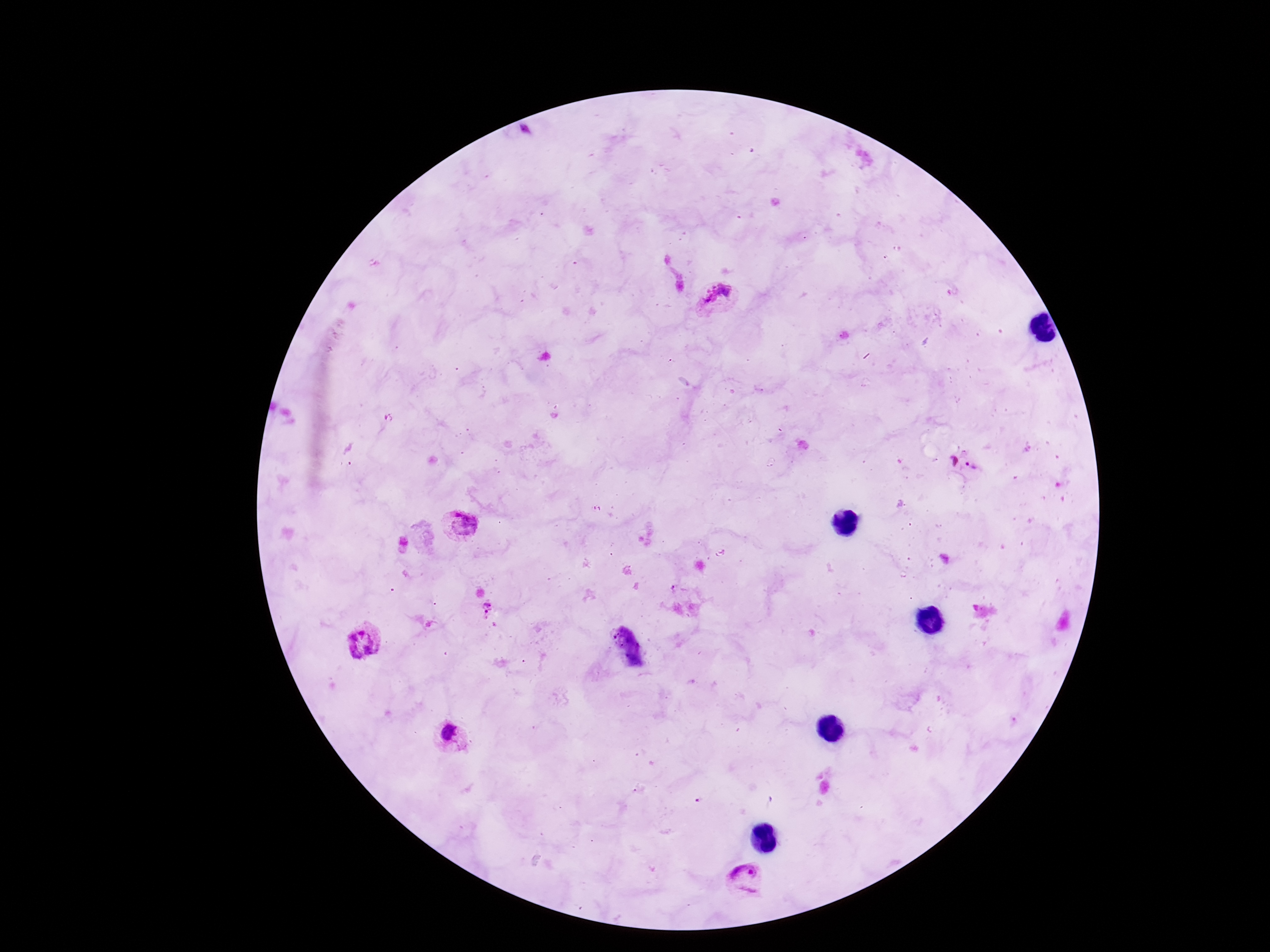
Approximate object centers, in pixels from the top-left corner.
Summary:
  - Plasmodium parasite locations: (x=716, y=300), (x=963, y=464), (x=459, y=526), (x=363, y=640), (x=452, y=739), (x=746, y=881)
  - Preparation: thick blood smear
  - Patient malaria status: positive
  - Stain: Giemsa
  - Image size: 1270×952 pixels
  - Magnification: 100x
  - Capture: smartphone camera through the microscope eyepiece
  - Field of view: one from this slide